Classify this cell by malaria status.
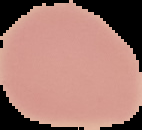
Uninfected.

{
  "image_type": "segmented cell region with the area outside set to black",
  "image_size": "142×130 pixels",
  "preparation": "thin blood film"
}